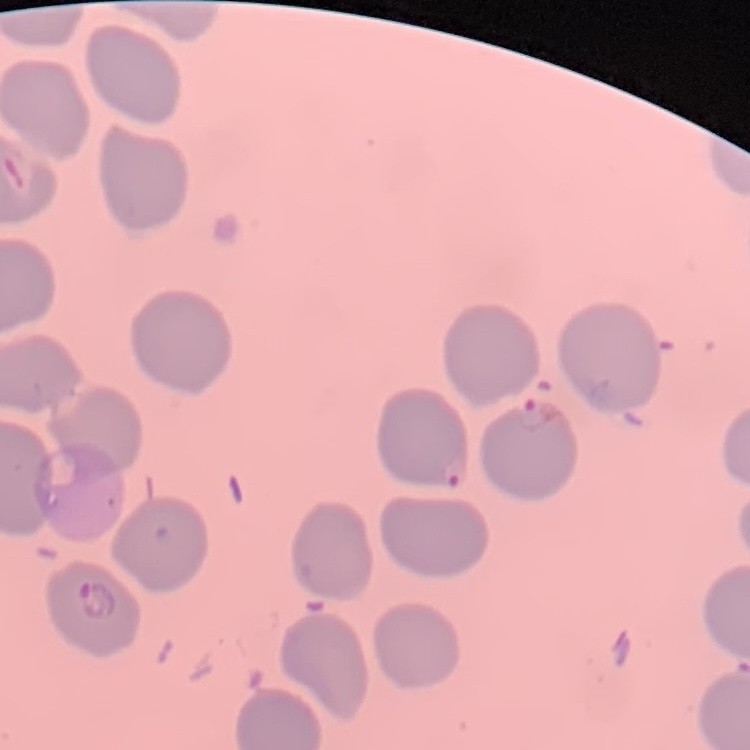
erythrocyte morphology = no rouleaux formation
stain = Field's or Giemsa
image type = one tile cut from a larger photomicrograph
preparation = thin peripheral smear